Give the extent of all Plasmodium vivax-infected red blood cells.
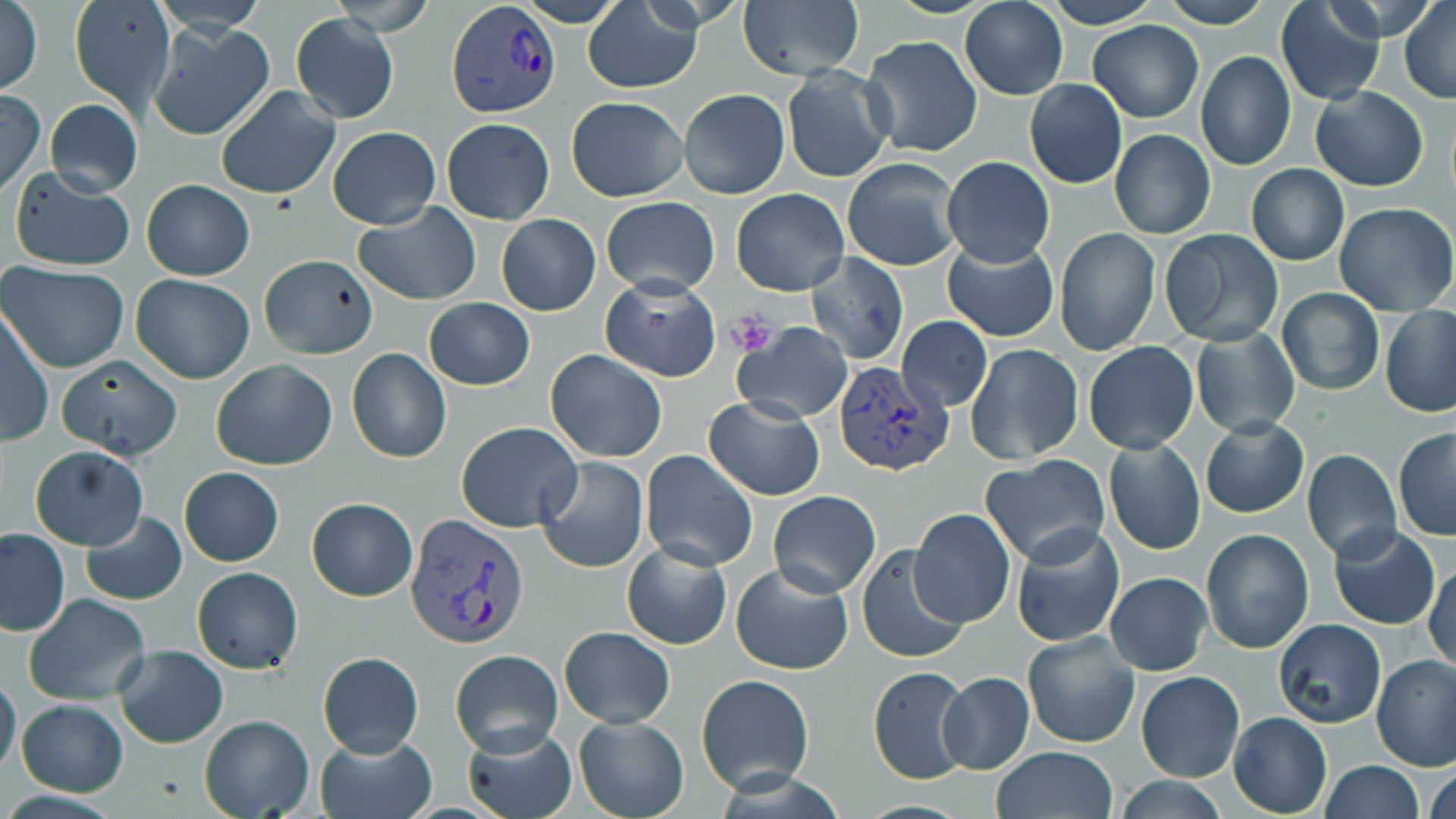

Approximate bounding boxes as named x1/y1/x2/y2 corners in pixels.
Plasmodium vivax-infected red blood cells: (x1=450, y1=2, x2=561, y2=118), (x1=833, y1=358, x2=954, y2=477), (x1=405, y1=513, x2=528, y2=649).

Summary:
  - Platelet locations: (x1=729, y1=312, x2=775, y2=356)
  - Uninfected red blood cell locations: (x1=69, y1=0, x2=174, y2=111), (x1=738, y1=0, x2=864, y2=82), (x1=959, y1=0, x2=1069, y2=100), (x1=1039, y1=0, x2=1165, y2=28), (x1=1159, y1=0, x2=1274, y2=27), (x1=1400, y1=0, x2=1456, y2=103), (x1=1, y1=1, x2=43, y2=97), (x1=1275, y1=1, x2=1387, y2=106), (x1=582, y1=3, x2=701, y2=93), (x1=291, y1=12, x2=398, y2=123), (x1=1088, y1=20, x2=1205, y2=123), (x1=147, y1=21, x2=274, y2=141), (x1=861, y1=34, x2=983, y2=159), (x1=1196, y1=50, x2=1295, y2=171), (x1=782, y1=68, x2=893, y2=182), (x1=1024, y1=78, x2=1128, y2=190), (x1=216, y1=86, x2=340, y2=198), (x1=1311, y1=86, x2=1428, y2=192), (x1=679, y1=88, x2=790, y2=199), (x1=0, y1=90, x2=46, y2=198), (x1=566, y1=96, x2=687, y2=202), (x1=44, y1=99, x2=142, y2=199), (x1=441, y1=119, x2=555, y2=224), (x1=328, y1=125, x2=440, y2=230), (x1=1109, y1=129, x2=1217, y2=240), (x1=942, y1=156, x2=1055, y2=267), (x1=843, y1=158, x2=962, y2=272), (x1=10, y1=164, x2=136, y2=272), (x1=1246, y1=164, x2=1349, y2=265), (x1=143, y1=179, x2=254, y2=280), (x1=731, y1=189, x2=851, y2=295), (x1=601, y1=196, x2=720, y2=297), (x1=1334, y1=201, x2=1455, y2=315), (x1=354, y1=202, x2=482, y2=305), (x1=496, y1=214, x2=600, y2=315), (x1=1055, y1=227, x2=1160, y2=357), (x1=1160, y1=228, x2=1284, y2=348), (x1=942, y1=237, x2=1059, y2=343), (x1=803, y1=253, x2=909, y2=366), (x1=259, y1=257, x2=380, y2=358), (x1=1, y1=262, x2=130, y2=372), (x1=131, y1=273, x2=255, y2=384), (x1=600, y1=277, x2=721, y2=383), (x1=1277, y1=288, x2=1383, y2=395), (x1=423, y1=297, x2=534, y2=390), (x1=1380, y1=305, x2=1456, y2=417), (x1=1, y1=307, x2=52, y2=446), (x1=897, y1=315, x2=993, y2=413), (x1=732, y1=323, x2=853, y2=423), (x1=1190, y1=328, x2=1301, y2=439), (x1=1082, y1=341, x2=1199, y2=454), (x1=966, y1=343, x2=1084, y2=464), (x1=346, y1=347, x2=452, y2=463), (x1=545, y1=351, x2=668, y2=463), (x1=55, y1=355, x2=184, y2=460), (x1=211, y1=359, x2=338, y2=470), (x1=703, y1=396, x2=826, y2=502), (x1=1201, y1=416, x2=1310, y2=519), (x1=456, y1=421, x2=582, y2=531), (x1=1393, y1=428, x2=1456, y2=539), (x1=1103, y1=439, x2=1207, y2=555), (x1=30, y1=446, x2=149, y2=550), (x1=640, y1=450, x2=758, y2=571), (x1=1302, y1=450, x2=1401, y2=563), (x1=980, y1=454, x2=1111, y2=569), (x1=536, y1=456, x2=648, y2=573), (x1=179, y1=468, x2=284, y2=566), (x1=768, y1=490, x2=880, y2=597), (x1=305, y1=498, x2=417, y2=601), (x1=908, y1=507, x2=1016, y2=629), (x1=79, y1=511, x2=189, y2=606), (x1=1010, y1=525, x2=1123, y2=648), (x1=1329, y1=525, x2=1440, y2=630), (x1=0, y1=528, x2=70, y2=635), (x1=1201, y1=529, x2=1314, y2=653), (x1=622, y1=542, x2=732, y2=649), (x1=856, y1=546, x2=970, y2=663), (x1=730, y1=562, x2=854, y2=675), (x1=1426, y1=562, x2=1456, y2=674), (x1=192, y1=567, x2=304, y2=674), (x1=1104, y1=572, x2=1213, y2=676), (x1=24, y1=594, x2=152, y2=706), (x1=1274, y1=620, x2=1386, y2=730), (x1=559, y1=626, x2=675, y2=728), (x1=1022, y1=630, x2=1142, y2=748), (x1=112, y1=645, x2=228, y2=749), (x1=450, y1=649, x2=563, y2=756), (x1=316, y1=651, x2=424, y2=758), (x1=1372, y1=654, x2=1456, y2=770), (x1=867, y1=665, x2=975, y2=784), (x1=1136, y1=670, x2=1244, y2=783), (x1=939, y1=672, x2=1034, y2=774), (x1=696, y1=673, x2=816, y2=794), (x1=0, y1=674, x2=22, y2=779), (x1=17, y1=698, x2=129, y2=797), (x1=1228, y1=712, x2=1331, y2=817), (x1=574, y1=714, x2=688, y2=819), (x1=199, y1=715, x2=315, y2=819), (x1=462, y1=725, x2=578, y2=819), (x1=315, y1=734, x2=437, y2=819), (x1=989, y1=747, x2=1119, y2=819), (x1=1317, y1=761, x2=1424, y2=819), (x1=1425, y1=761, x2=1455, y2=819), (x1=1111, y1=777, x2=1233, y2=819)
  - Slide-level diagnosis: Plasmodium vivax
  - Image size: 1456×819 pixels
  - Magnification: 1000x
  - Modality: light microscopy
  - Preparation: thin blood film
  - Stain: May-Grünwald-Giemsa
  - Field of view: single